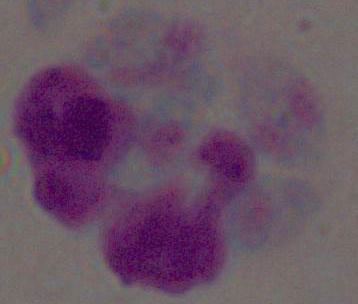

identification = white blood cell
magnification = 1000x
modality = photomicrograph